Locate every Trypanosoma brucei.
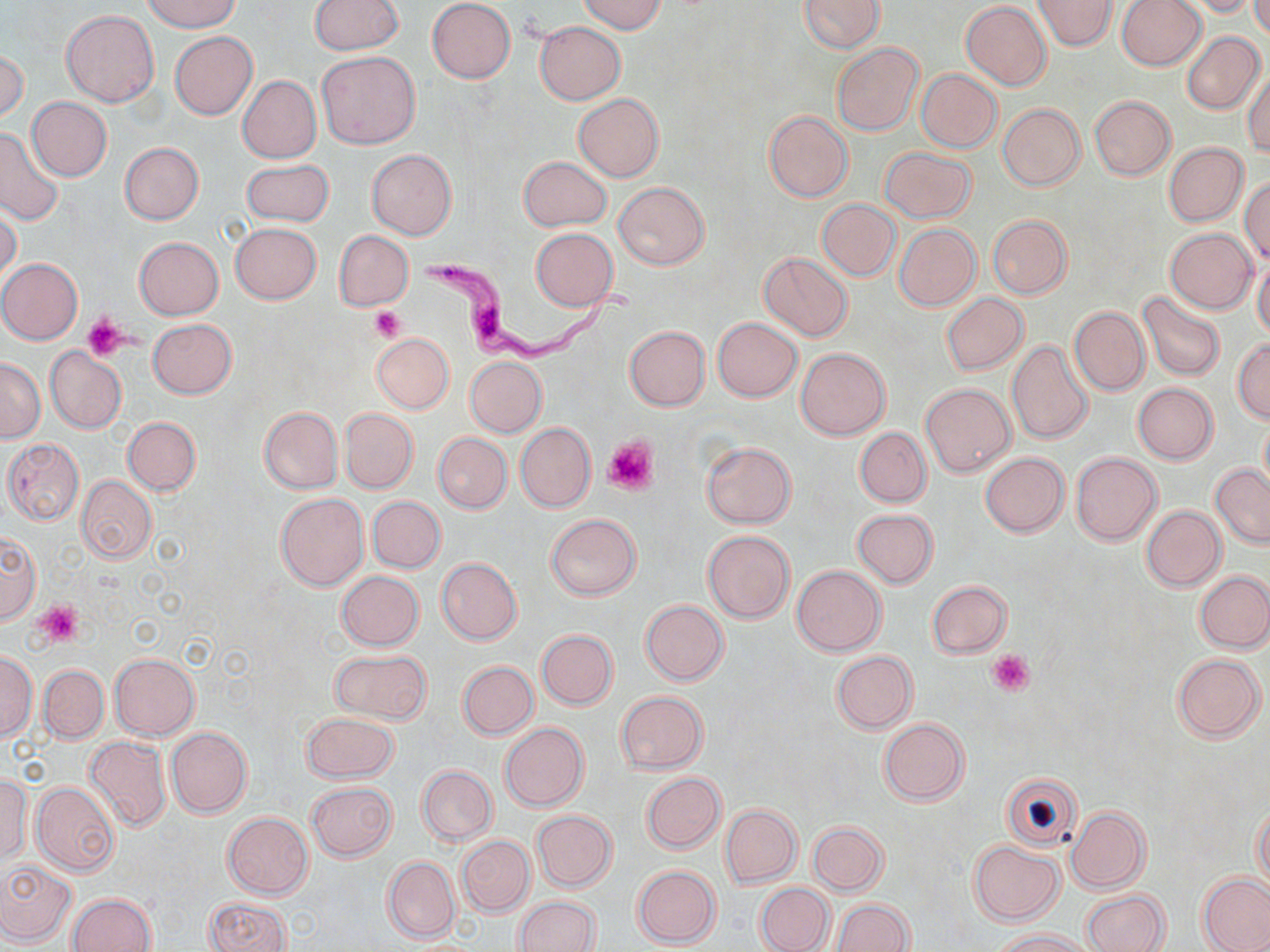
Approximate bounding boxes as named x1/y1/x2/y2 corners in pixels.
Trypanosoma brucei: (x1=418, y1=251, x2=634, y2=372).

slide-level diagnosis = Trypanosoma brucei
platelet locations = approximate bounding boxes as named x1/y1/x2/y2 corners in pixels: (x1=369, y1=306, x2=405, y2=343), (x1=83, y1=316, x2=127, y2=361), (x1=604, y1=436, x2=659, y2=495), (x1=34, y1=601, x2=83, y2=644), (x1=988, y1=649, x2=1035, y2=696)
uninfected red blood cell locations = approximate bounding boxes as named x1/y1/x2/y2 corners in pixels: (x1=145, y1=0, x2=240, y2=32), (x1=576, y1=0, x2=666, y2=34), (x1=798, y1=0, x2=886, y2=53), (x1=1034, y1=0, x2=1116, y2=50), (x1=1117, y1=0, x2=1206, y2=70), (x1=1185, y1=0, x2=1259, y2=18), (x1=1249, y1=0, x2=1270, y2=40), (x1=310, y1=1, x2=403, y2=54), (x1=427, y1=1, x2=516, y2=83), (x1=961, y1=2, x2=1052, y2=89), (x1=59, y1=10, x2=159, y2=107), (x1=533, y1=21, x2=626, y2=104), (x1=169, y1=31, x2=257, y2=119), (x1=1182, y1=31, x2=1266, y2=115), (x1=832, y1=43, x2=923, y2=136), (x1=1, y1=47, x2=28, y2=126), (x1=316, y1=51, x2=420, y2=149), (x1=1243, y1=66, x2=1270, y2=157), (x1=915, y1=69, x2=1002, y2=152), (x1=238, y1=75, x2=321, y2=162), (x1=573, y1=94, x2=664, y2=182), (x1=1089, y1=96, x2=1175, y2=180), (x1=27, y1=97, x2=112, y2=181), (x1=998, y1=103, x2=1085, y2=190), (x1=764, y1=111, x2=852, y2=202), (x1=0, y1=127, x2=64, y2=225), (x1=119, y1=142, x2=204, y2=225), (x1=1164, y1=142, x2=1249, y2=226), (x1=880, y1=147, x2=974, y2=222), (x1=366, y1=149, x2=457, y2=240), (x1=518, y1=156, x2=611, y2=231), (x1=242, y1=159, x2=333, y2=227), (x1=1241, y1=176, x2=1270, y2=265), (x1=614, y1=183, x2=709, y2=269), (x1=818, y1=200, x2=900, y2=280), (x1=0, y1=203, x2=22, y2=290), (x1=988, y1=214, x2=1072, y2=298), (x1=230, y1=223, x2=321, y2=304), (x1=894, y1=224, x2=981, y2=310), (x1=530, y1=228, x2=618, y2=310), (x1=1165, y1=229, x2=1257, y2=313), (x1=334, y1=230, x2=413, y2=310), (x1=134, y1=237, x2=223, y2=320), (x1=758, y1=252, x2=853, y2=341), (x1=1253, y1=255, x2=1270, y2=343), (x1=0, y1=258, x2=83, y2=345), (x1=1139, y1=291, x2=1225, y2=381), (x1=941, y1=293, x2=1028, y2=375), (x1=1068, y1=306, x2=1149, y2=397), (x1=713, y1=317, x2=801, y2=401), (x1=148, y1=319, x2=237, y2=399), (x1=624, y1=326, x2=710, y2=411), (x1=371, y1=334, x2=454, y2=413), (x1=1006, y1=340, x2=1094, y2=444), (x1=1233, y1=340, x2=1269, y2=424), (x1=44, y1=346, x2=127, y2=434), (x1=796, y1=348, x2=890, y2=439), (x1=465, y1=356, x2=546, y2=437), (x1=0, y1=359, x2=45, y2=443), (x1=921, y1=383, x2=1015, y2=476), (x1=1133, y1=383, x2=1218, y2=463), (x1=258, y1=406, x2=343, y2=494), (x1=340, y1=408, x2=418, y2=493), (x1=123, y1=416, x2=200, y2=496), (x1=1259, y1=417, x2=1270, y2=497), (x1=515, y1=423, x2=595, y2=512), (x1=855, y1=427, x2=930, y2=506), (x1=433, y1=432, x2=512, y2=513), (x1=3, y1=439, x2=84, y2=525), (x1=702, y1=442, x2=796, y2=528), (x1=980, y1=452, x2=1069, y2=537), (x1=1071, y1=452, x2=1161, y2=544), (x1=1210, y1=464, x2=1270, y2=547), (x1=76, y1=476, x2=156, y2=563), (x1=275, y1=492, x2=369, y2=590), (x1=367, y1=496, x2=445, y2=573), (x1=1140, y1=504, x2=1225, y2=591), (x1=852, y1=508, x2=938, y2=587), (x1=546, y1=513, x2=640, y2=600), (x1=703, y1=530, x2=795, y2=623), (x1=0, y1=532, x2=39, y2=625), (x1=436, y1=558, x2=522, y2=644), (x1=792, y1=565, x2=886, y2=655), (x1=1196, y1=570, x2=1270, y2=653), (x1=336, y1=571, x2=424, y2=652), (x1=927, y1=579, x2=1012, y2=658), (x1=640, y1=599, x2=729, y2=686), (x1=536, y1=629, x2=618, y2=709), (x1=330, y1=649, x2=432, y2=724), (x1=0, y1=651, x2=37, y2=741), (x1=831, y1=651, x2=918, y2=734), (x1=108, y1=652, x2=200, y2=740), (x1=1172, y1=654, x2=1265, y2=742), (x1=457, y1=660, x2=538, y2=739), (x1=38, y1=664, x2=108, y2=742), (x1=615, y1=691, x2=709, y2=773), (x1=301, y1=713, x2=398, y2=783), (x1=879, y1=717, x2=969, y2=805), (x1=499, y1=722, x2=588, y2=812), (x1=166, y1=727, x2=252, y2=818), (x1=84, y1=735, x2=172, y2=832), (x1=417, y1=765, x2=497, y2=846), (x1=0, y1=772, x2=32, y2=863), (x1=1001, y1=772, x2=1082, y2=850), (x1=642, y1=773, x2=726, y2=853), (x1=30, y1=782, x2=119, y2=877), (x1=307, y1=782, x2=396, y2=861), (x1=1252, y1=803, x2=1270, y2=890), (x1=721, y1=804, x2=801, y2=887), (x1=1066, y1=806, x2=1149, y2=893), (x1=532, y1=811, x2=617, y2=892), (x1=222, y1=813, x2=314, y2=898), (x1=807, y1=821, x2=888, y2=895), (x1=457, y1=836, x2=535, y2=916), (x1=968, y1=841, x2=1064, y2=926), (x1=383, y1=856, x2=460, y2=943), (x1=0, y1=858, x2=77, y2=946), (x1=632, y1=865, x2=721, y2=948), (x1=1197, y1=873, x2=1270, y2=952), (x1=755, y1=882, x2=833, y2=952), (x1=1082, y1=889, x2=1169, y2=952), (x1=68, y1=892, x2=156, y2=952), (x1=514, y1=897, x2=601, y2=952), (x1=204, y1=898, x2=291, y2=952), (x1=831, y1=899, x2=913, y2=952), (x1=991, y1=928, x2=1092, y2=951)
magnification = 1000x
stain = May-Grünwald-Giemsa
modality = light microscopy
field of view = single
image size = 1270×952 pixels
preparation = thin blood smear